Identify the preparation type.
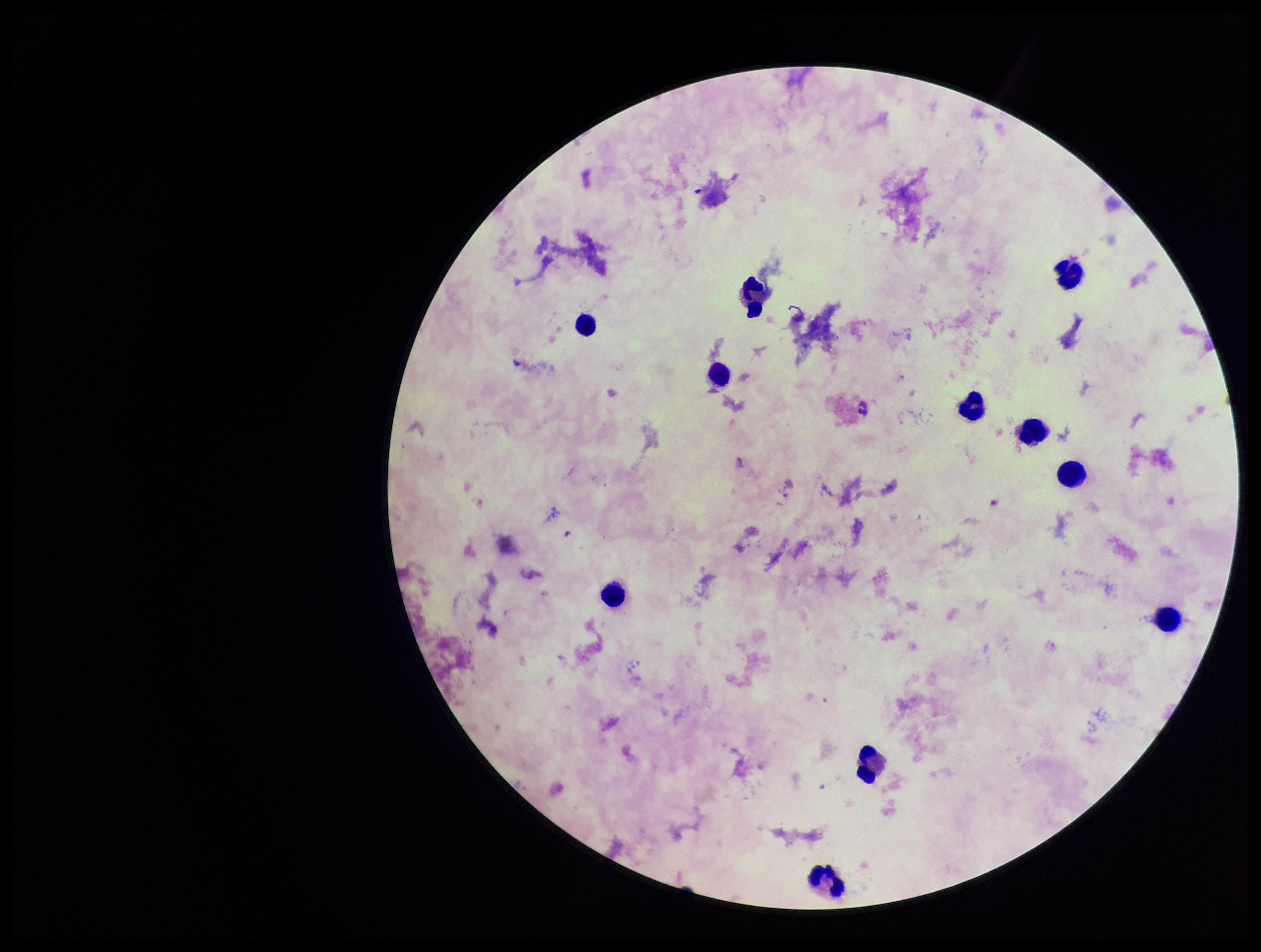
Thick.

Image is 1261×952 pixels. Smartphone photograph taken through the eyepiece of a microscope. Leukocyte count: 11. Parasite count: 2. Patient malaria status: infected. One field from this slide. Species reported for this patient: Plasmodium falciparum. Giemsa stain. Plasmodium parasites: identified.